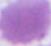 Captured at 1000x magnification. Micrograph. An erythrocyte is shown.